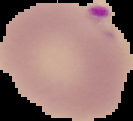
Segmented cell region on a black background. Image is 133×121 pixels. From a thin blood film. Malaria status: parasitized.